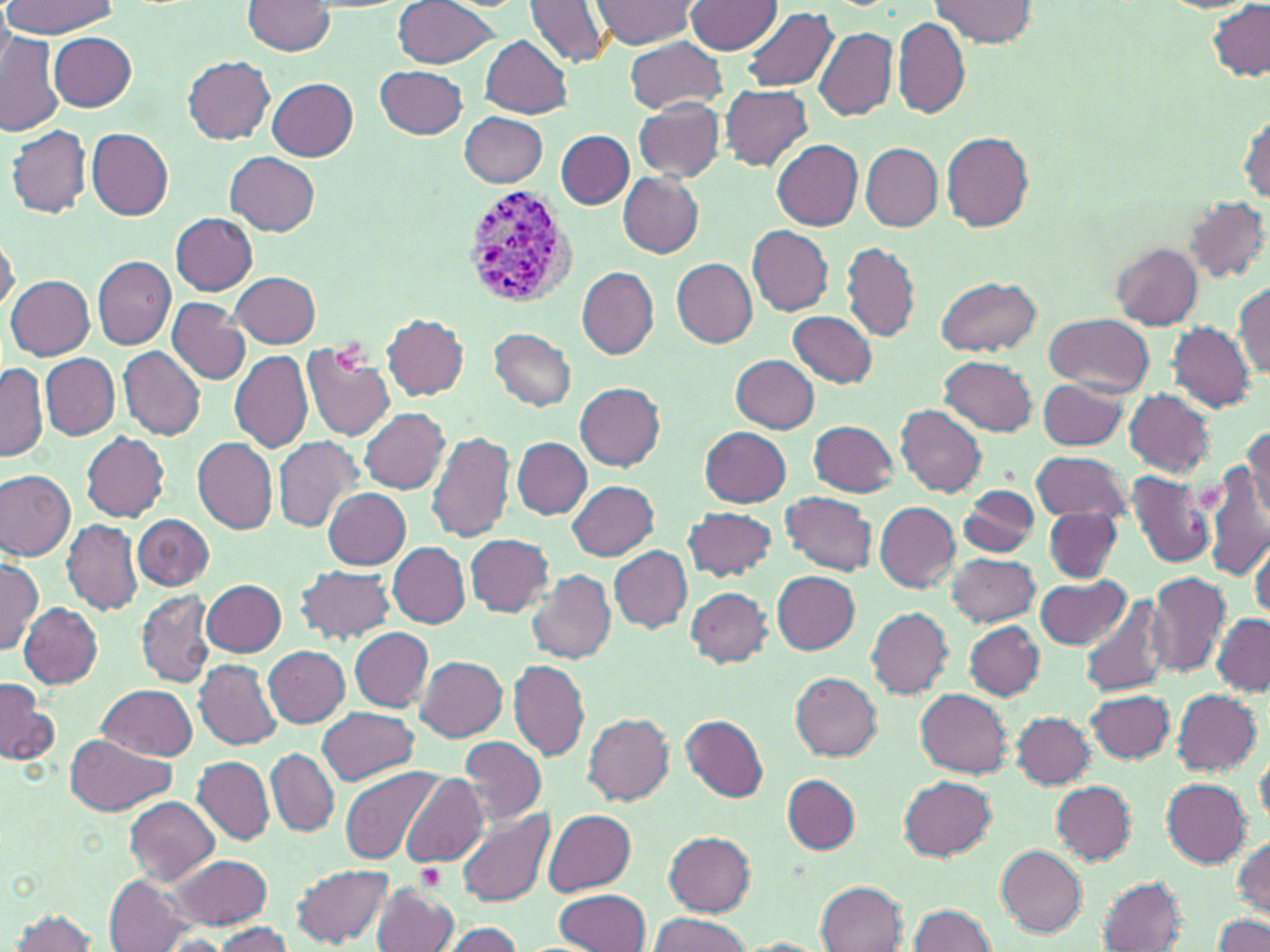
Summary:
  - Coordinate format: approximate bounding boxes as (x1,y1)-(x2,y2) corner pairs in pixels
  - Plasmodium vivax-infected red blood cell locations: (462,182)-(578,310)
  - Uninfected red blood cell locations: (392,0)-(500,69), (524,0)-(610,68), (592,0)-(695,48), (687,0)-(783,54), (932,0)-(1035,47), (243,1)-(337,57), (3,2)-(120,37), (1207,2)-(1270,81), (740,6)-(837,93), (892,17)-(969,119), (812,27)-(896,121), (0,32)-(64,137), (48,32)-(138,111), (482,36)-(571,118), (625,36)-(728,114), (183,56)-(274,144), (376,65)-(467,139), (267,78)-(357,161), (720,85)-(812,171), (633,98)-(724,182), (1238,110)-(1269,205), (459,112)-(548,188), (7,123)-(91,217), (86,127)-(174,218), (557,131)-(633,209), (941,133)-(1035,231), (773,140)-(863,231), (861,143)-(941,230), (226,152)-(319,235), (618,173)-(703,257), (1183,196)-(1268,283), (170,212)-(258,293), (746,225)-(833,315), (0,232)-(18,314), (842,242)-(919,342), (1110,243)-(1203,329), (92,256)-(174,349), (672,259)-(757,347), (576,266)-(658,359), (232,272)-(320,348), (6,275)-(96,358), (935,277)-(1042,357), (1234,280)-(1270,380), (166,298)-(251,385), (788,310)-(878,388), (382,314)-(470,399), (1045,314)-(1155,395), (1168,322)-(1257,412), (490,328)-(576,411), (302,343)-(396,441), (119,346)-(207,439), (229,350)-(313,453), (42,353)-(119,440), (730,354)-(819,434), (941,355)-(1039,435), (1,363)-(46,463), (1037,379)-(1127,449), (575,383)-(665,470), (1124,389)-(1214,478), (897,404)-(987,497), (360,407)-(450,495), (808,419)-(898,496), (1243,425)-(1270,519), (700,426)-(792,506), (425,430)-(516,544), (82,432)-(170,521), (272,435)-(364,533), (192,438)-(278,535), (513,438)-(590,518), (1030,450)-(1132,523), (1205,464)-(1270,583), (0,470)-(76,560), (1125,470)-(1213,569), (567,480)-(658,560), (960,485)-(1039,556), (324,488)-(412,568), (780,491)-(877,576), (874,502)-(961,590), (682,507)-(777,580), (1042,507)-(1121,581), (133,514)-(213,590), (62,518)-(143,615), (465,535)-(556,615), (1249,540)-(1269,621), (389,542)-(469,628), (610,546)-(692,632), (947,554)-(1039,626), (0,561)-(41,656), (296,566)-(395,644), (527,568)-(616,664), (772,570)-(860,654), (1146,571)-(1230,679), (1034,575)-(1129,650), (201,578)-(286,657), (684,587)-(772,666), (136,591)-(214,688), (1079,592)-(1171,697), (18,602)-(102,688), (865,606)-(952,697), (1210,615)-(1270,696), (964,621)-(1043,699), (349,628)-(433,711), (332,630)-(437,780), (265,645)-(350,728), (416,657)-(508,741), (195,659)-(282,749), (508,660)-(587,761), (791,672)-(883,760), (0,677)-(57,766), (96,684)-(197,759), (1171,688)-(1261,776), (915,689)-(1011,777), (1086,690)-(1175,764), (318,706)-(417,785), (1010,711)-(1096,789), (583,713)-(674,805), (682,715)-(768,801), (65,733)-(175,815), (459,736)-(546,828), (1256,745)-(1270,826), (267,749)-(338,837), (193,755)-(274,845), (341,767)-(444,866), (783,774)-(859,854), (399,775)-(488,868), (900,775)-(996,861), (1160,777)-(1252,867), (1050,781)-(1136,864), (125,797)-(219,884), (455,809)-(555,907), (544,809)-(637,895), (663,830)-(756,915), (1232,837)-(1270,918), (996,845)-(1087,938), (168,853)-(271,930), (292,863)-(393,947), (1097,876)-(1187,952), (105,877)-(196,951), (372,880)-(461,952), (816,880)-(907,951), (550,890)-(651,951), (908,905)-(997,952), (8,908)-(101,951), (1214,912)-(1270,952), (649,913)-(753,952), (439,922)-(526,951), (207,924)-(294,952), (741,938)-(828,952)
  - Platelet locations: (417,863)-(446,892)
  - Slide-level diagnosis: Plasmodium vivax
  - Preparation: thin blood smear
  - Modality: optical microscopy
  - Image size: 1270×952 pixels
  - Field of view: single
  - Magnification: 1000x
  - Stain: May-Grünwald-Giemsa